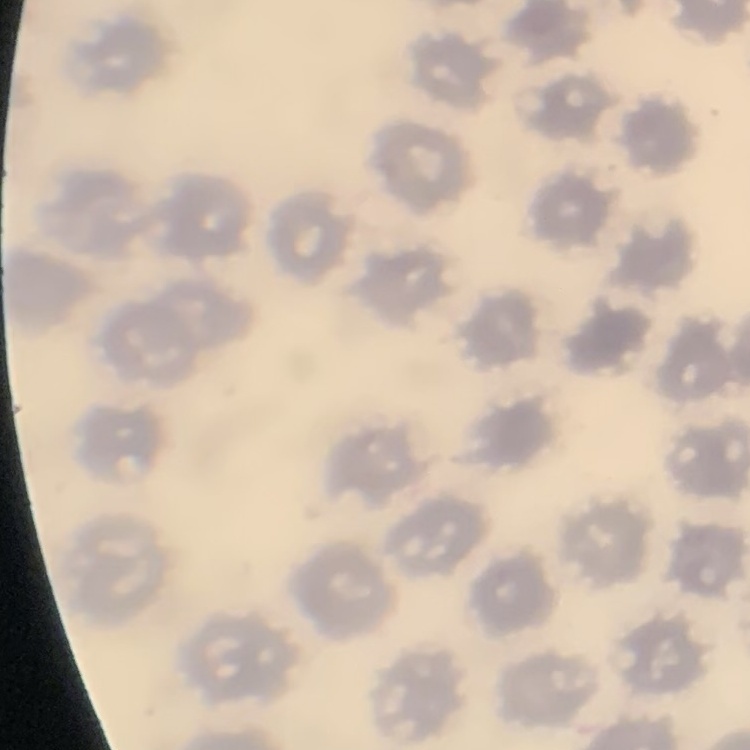
The red blood cells exhibit no rouleaux formation. One tile cut from a larger photomicrograph. Stained with either Field's or Giemsa. Thin blood film.